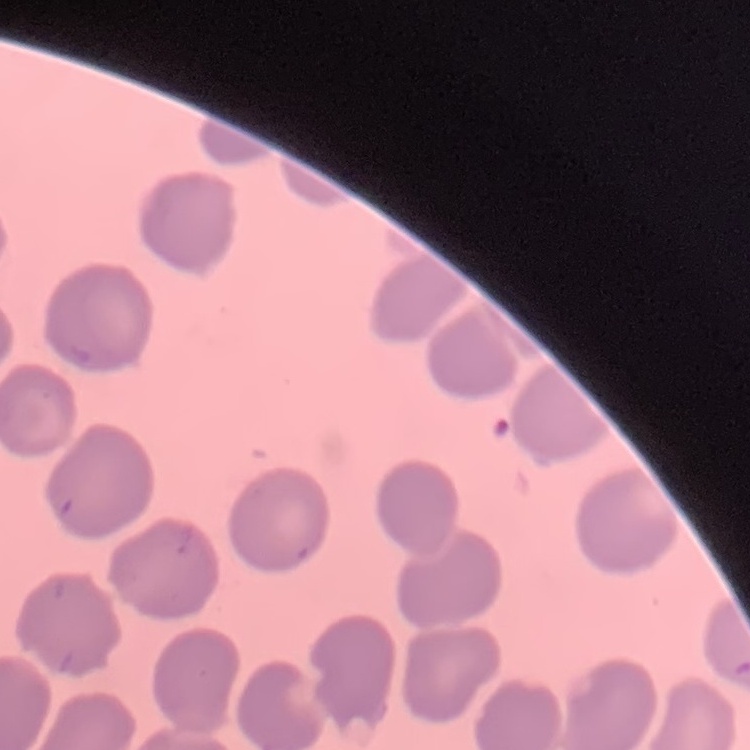

Summary:
  - Erythrocyte morphology: no rouleaux formation
  - Image type: square crop of a larger photomicrograph
  - Preparation: thin peripheral smear
  - Stain: Field's or Giemsa